Locate every malaria parasite.
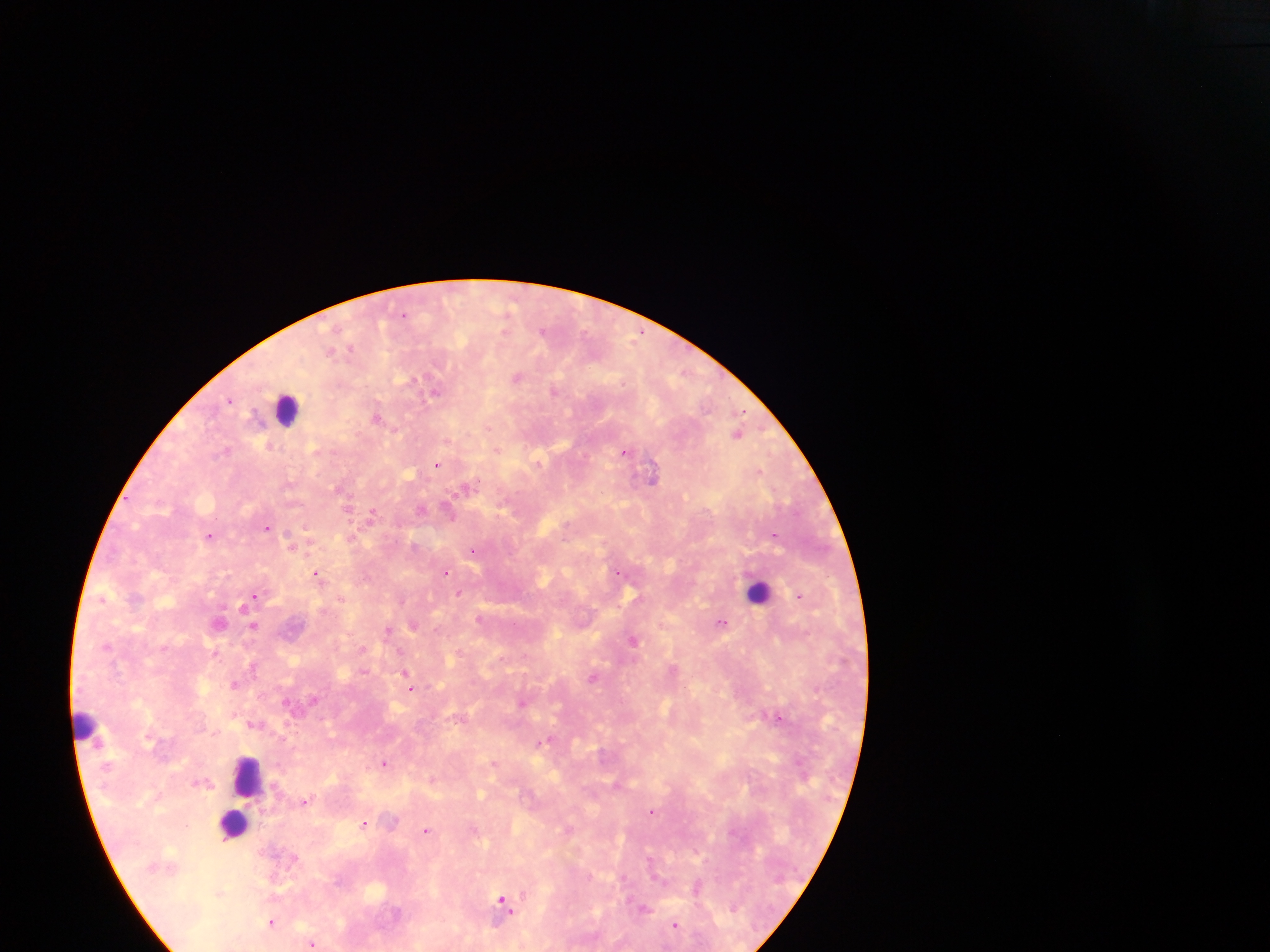
Approximate centers as [x, y] in pixels.
Malaria parasites: [508, 311], [403, 315], [542, 331], [640, 333], [350, 348], [330, 351], [517, 377], [554, 391], [436, 392], [230, 399], [377, 418], [487, 428], [738, 433], [226, 450], [498, 450], [626, 451], [539, 462], [437, 464], [652, 476], [474, 484], [420, 509], [449, 513], [371, 514], [267, 528], [209, 535], [775, 536], [291, 543], [474, 550], [446, 572], [617, 572], [317, 574], [460, 594], [254, 595], [801, 596], [102, 598], [402, 600], [242, 606], [478, 617], [218, 622], [721, 622], [414, 624], [254, 626], [388, 631], [633, 639], [459, 652], [216, 653], [252, 666], [364, 672], [405, 672], [594, 678], [407, 681], [235, 685], [410, 688], [522, 703], [780, 717], [541, 742], [384, 763], [494, 763], [617, 785], [304, 801], [652, 811], [364, 823], [569, 828], [426, 830], [696, 888], [502, 901], [644, 908], [271, 922], [674, 925], [311, 944].

Leukocyte locations: [287, 408], [759, 591], [86, 723], [248, 775], [233, 823]. Sample from Ghana. Photographed through a microscope with a mobile-phone camera. Single field of view. Image is 1270×952 pixels. Thick blood film.